State which cell type is depicted.
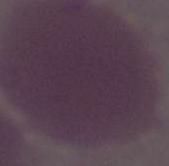
This is an erythrocyte.

Captured at 1000x magnification. Micrograph.